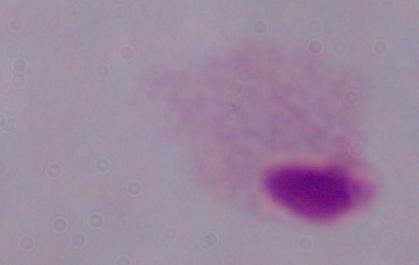

Summary:
  - Modality: photomicrograph
  - Identification: trichomonad
  - Magnification: 1000x